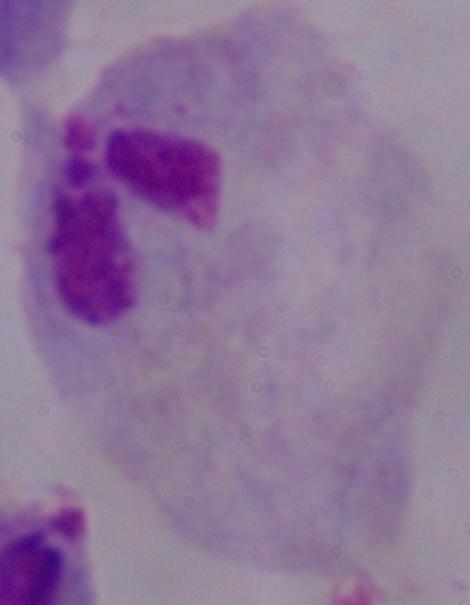
A trichomonad is seen. Photomicrograph. Captured at 1000x magnification.